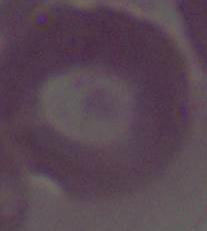

identification = erythrocyte
modality = micrograph
magnification = 1000x